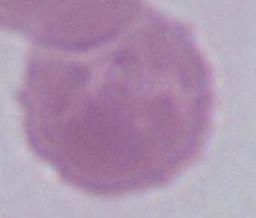
magnification = 1000x
modality = photomicrograph
identification = erythrocyte